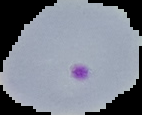
Image is 142×115 pixels. Cell region segmented out of the field of view; the surrounding area is masked to black. From a thin blood film. Malaria status: parasitized.